Assess this cell for malaria.
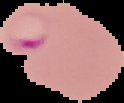

It is parasitized.

The area outside the segmented cell region is set to black. Image is 124×103 pixels. From a thin blood film.